Classify this cell by malaria status.
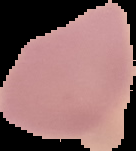

Uninfected.

image size = 136×151 pixels
preparation = thin blood film
image type = segmented cell region on a black background